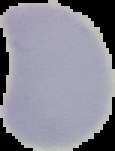

preparation = thin blood film
image size = 115×151 pixels
image type = segmented cell region on a black background
malaria status = uninfected